State which parasite is depicted.
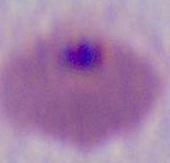
This is Plasmodium.

{
  "modality": "micrograph",
  "magnification": "400x or 1000x"
}